Locate every Plasmodium falciparum-infected red blood cell.
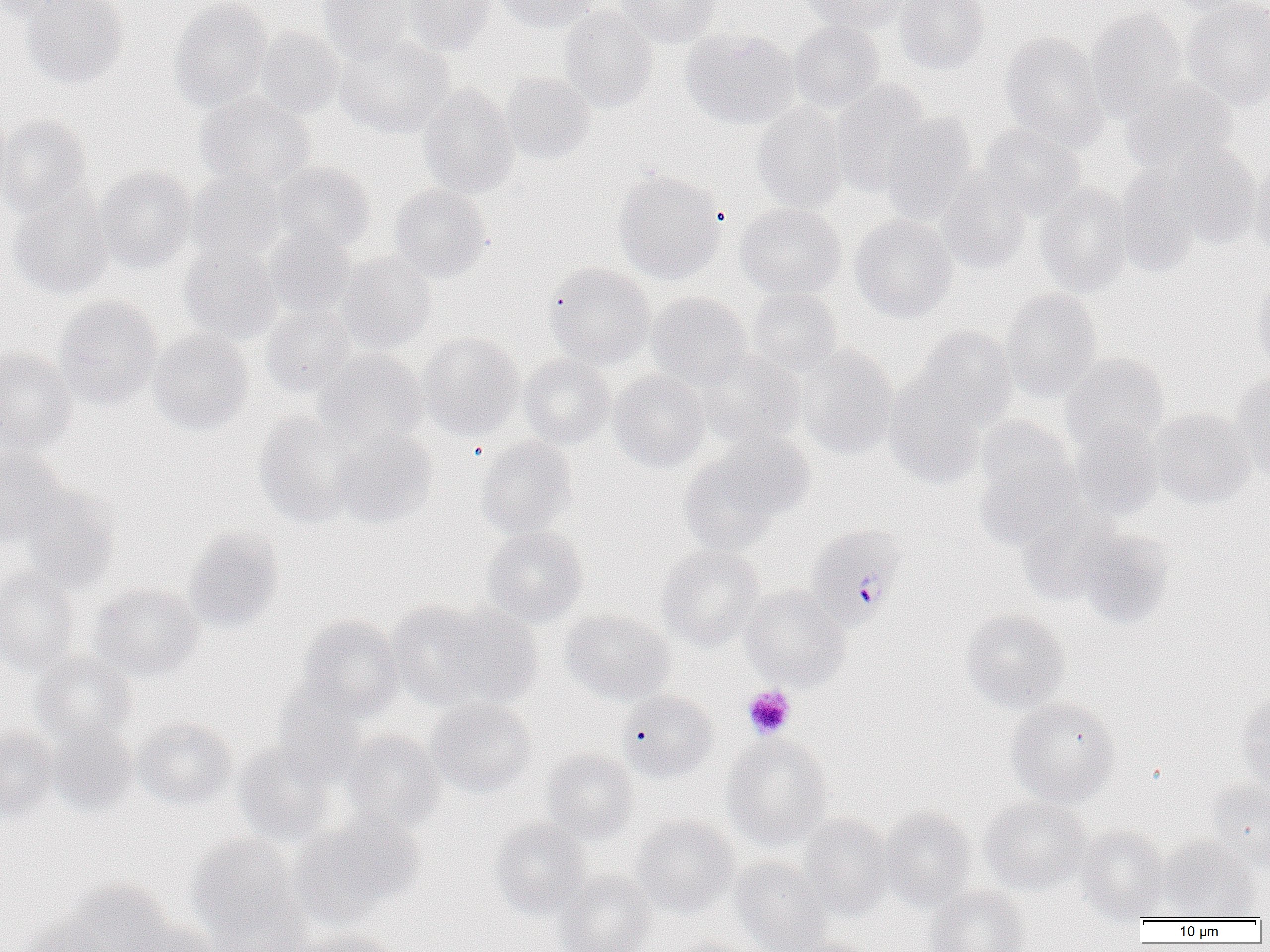
Approximate bounding boxes as (x1,y1)-(x2,y2) corner pairs in pixels.
Plasmodium falciparum-infected red blood cells: (804,523)-(908,629).

Summary:
  - Platelet locations: (742,685)-(796,740)
  - Uninfected red blood cell locations: (0,0)-(87,22), (21,0)-(128,89), (169,0)-(272,111), (403,0)-(498,55), (494,0)-(598,32), (615,0)-(722,48), (803,0)-(912,34), (894,0)-(991,74), (1168,0)-(1264,16), (1182,0)-(1270,110), (317,1)-(413,64), (558,5)-(658,112), (1086,10)-(1188,120), (788,20)-(884,113), (254,27)-(345,117), (680,28)-(800,130), (999,31)-(1109,150), (334,35)-(456,139), (500,72)-(596,163), (830,79)-(932,195), (1122,79)-(1238,174), (417,85)-(520,199), (196,93)-(315,188), (0,101)-(12,206), (751,101)-(850,213), (879,114)-(979,225), (0,115)-(92,222), (979,123)-(1086,220), (1161,142)-(1261,247), (1249,156)-(1270,262), (271,161)-(375,253), (95,166)-(196,273), (187,168)-(286,264), (613,169)-(727,284), (1113,170)-(1203,277), (937,171)-(1033,275), (389,182)-(492,282), (1035,184)-(1134,297), (7,194)-(113,299), (735,202)-(846,299), (849,215)-(958,322), (263,225)-(357,317), (178,242)-(283,346), (336,251)-(437,354), (544,262)-(655,369), (1251,279)-(1270,374), (746,288)-(842,378), (1001,288)-(1102,401), (647,292)-(752,387), (54,296)-(163,410), (260,303)-(357,397), (910,327)-(1018,433), (148,329)-(253,436), (417,333)-(525,440), (795,345)-(899,460), (0,347)-(77,455), (316,349)-(428,448), (695,351)-(805,449), (1060,353)-(1170,454), (518,354)-(615,449), (607,370)-(710,472), (1232,371)-(1270,479), (884,376)-(990,487), (1148,408)-(1256,508), (254,412)-(364,527), (973,418)-(1083,546), (1070,424)-(1164,521), (331,430)-(437,528), (475,436)-(577,539), (678,445)-(796,555), (0,447)-(68,545), (21,489)-(120,594), (1015,503)-(1125,606), (482,525)-(588,627), (184,527)-(284,632), (1074,528)-(1174,629), (656,543)-(765,649), (0,569)-(82,676), (88,582)-(204,681), (740,587)-(850,690), (387,599)-(537,713), (960,608)-(1070,713), (559,610)-(676,706), (298,614)-(404,721), (32,652)-(137,745), (272,680)-(372,784), (617,690)-(718,783), (1237,690)-(1270,790), (1006,697)-(1121,806), (426,698)-(537,798), (133,718)-(237,811), (46,723)-(138,816), (0,727)-(58,819), (340,730)-(445,835), (721,734)-(834,850), (233,743)-(339,848), (540,748)-(638,845), (1204,780)-(1270,869), (978,796)-(1091,895), (879,807)-(978,910), (291,812)-(424,928), (799,813)-(896,919), (630,816)-(738,916), (490,818)-(589,919), (1078,827)-(1171,921), (187,834)-(310,946), (1157,837)-(1262,921), (730,857)-(833,952), (554,870)-(656,952), (61,879)-(174,952), (925,883)-(1031,952), (14,919)-(112,952), (126,921)-(219,952), (291,928)-(404,952), (787,936)-(879,952), (663,938)-(760,952)
  - Slide-level diagnosis: Plasmodium falciparum
  - Magnification: 1000x
  - Preparation: thin blood smear
  - Image size: 1270×952 pixels
  - Field of view: single
  - Modality: optical microscopy